Name the cell type shown.
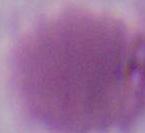
This is an erythrocyte.

modality = micrograph
magnification = 1000x